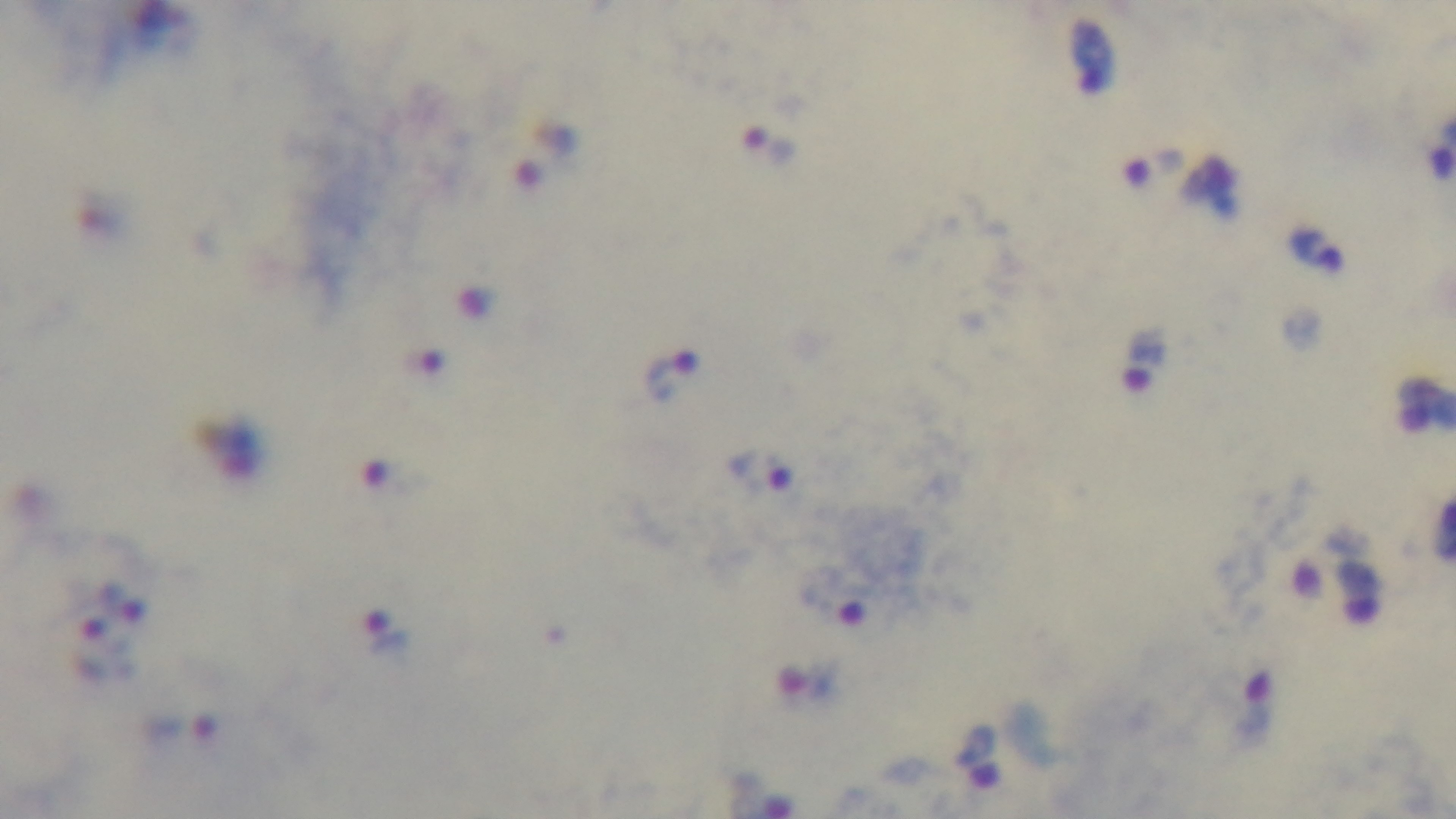
Single field of view. Preparation: thick blood film. Giemsa-stained. Mounted 4K digital camera. Oil-immersion objective, 100x. Malaria status: infected. Light microscopy.